Name the parasite shown.
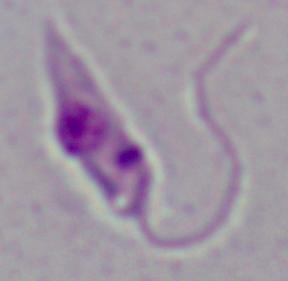
Leishmania.

magnification = 1000x
modality = photomicrograph